Classify this cell by malaria status.
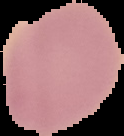

Uninfected.

From a thin blood smear. Segmented cell region on a black background. Image is 124×136 pixels.